Outline each Babesia divergens-infected red blood cell.
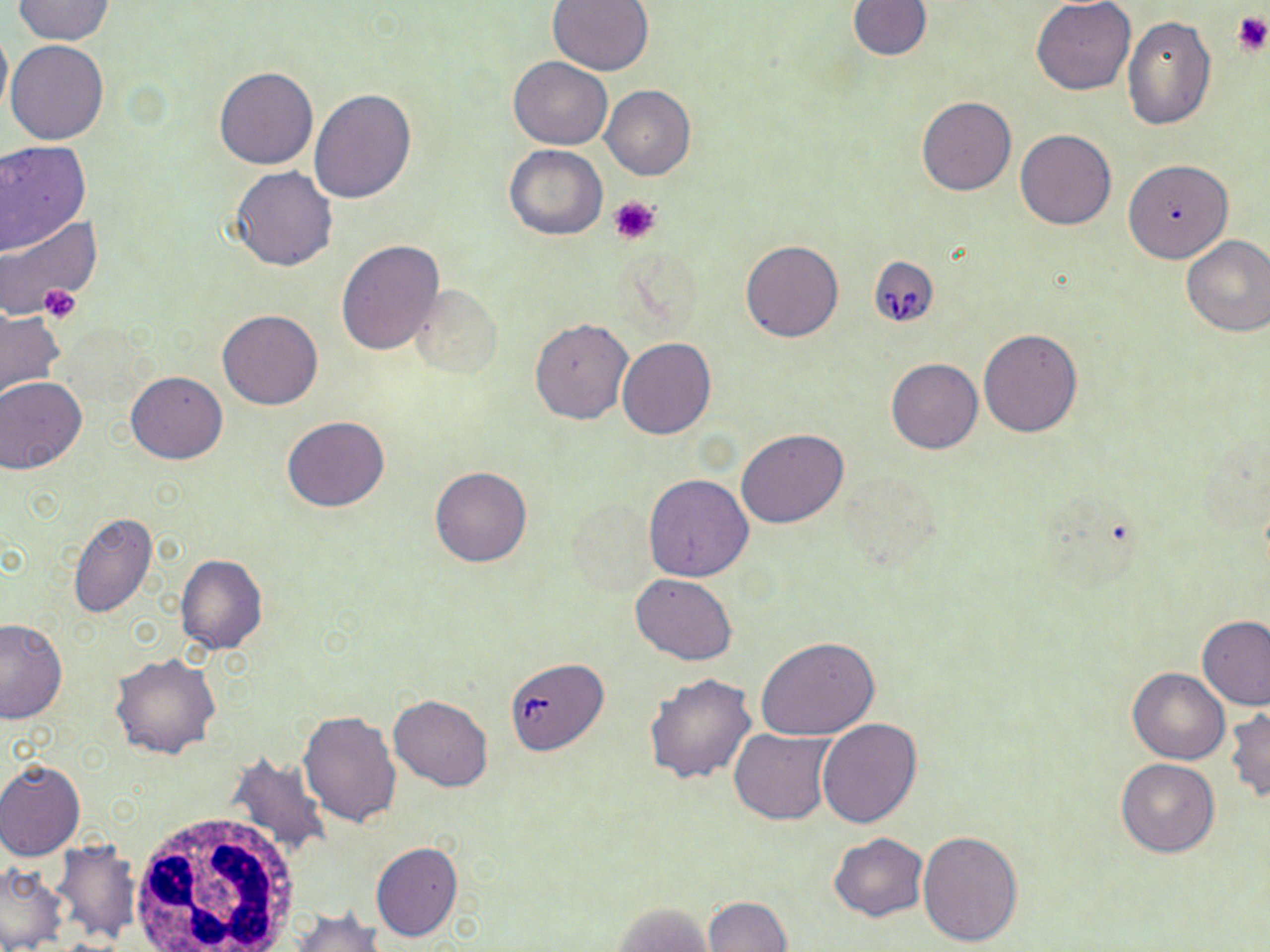
Approximate bounding boxes as named x1/y1/x2/y2 corners in pixels.
Babesia divergens-infected red blood cells: (x1=868, y1=256, x2=939, y2=328).

slide-level diagnosis = Babesia divergens
stain = May-Grünwald-Giemsa
platelet locations = approximate bounding boxes as named x1/y1/x2/y2 corners in pixels: (x1=1232, y1=10, x2=1269, y2=57), (x1=611, y1=196, x2=660, y2=244), (x1=37, y1=284, x2=82, y2=323)
field of view = single
modality = light microscopy
magnification = 1000x
uninfected red blood cell locations = approximate bounding boxes as named x1/y1/x2/y2 corners in pixels: (x1=849, y1=0, x2=932, y2=61), (x1=12, y1=1, x2=113, y2=45), (x1=546, y1=1, x2=654, y2=75), (x1=1031, y1=1, x2=1135, y2=96), (x1=1121, y1=17, x2=1216, y2=131), (x1=0, y1=23, x2=11, y2=127), (x1=6, y1=39, x2=109, y2=145), (x1=508, y1=56, x2=614, y2=149), (x1=214, y1=67, x2=317, y2=170), (x1=601, y1=85, x2=695, y2=180), (x1=309, y1=89, x2=417, y2=205), (x1=916, y1=96, x2=1016, y2=196), (x1=1015, y1=129, x2=1117, y2=230), (x1=0, y1=140, x2=90, y2=254), (x1=504, y1=144, x2=607, y2=241), (x1=1123, y1=160, x2=1232, y2=263), (x1=229, y1=166, x2=338, y2=271), (x1=0, y1=215, x2=105, y2=323), (x1=1180, y1=235, x2=1270, y2=338), (x1=740, y1=238, x2=844, y2=343), (x1=336, y1=239, x2=444, y2=355), (x1=411, y1=284, x2=500, y2=378), (x1=0, y1=306, x2=66, y2=401), (x1=217, y1=309, x2=324, y2=410), (x1=530, y1=318, x2=631, y2=424), (x1=979, y1=329, x2=1082, y2=437), (x1=616, y1=337, x2=715, y2=440), (x1=886, y1=357, x2=983, y2=454), (x1=126, y1=370, x2=228, y2=464), (x1=0, y1=377, x2=87, y2=475), (x1=282, y1=416, x2=391, y2=513), (x1=736, y1=427, x2=850, y2=528), (x1=430, y1=466, x2=531, y2=567), (x1=643, y1=474, x2=755, y2=582), (x1=68, y1=510, x2=158, y2=619), (x1=175, y1=554, x2=268, y2=655), (x1=631, y1=574, x2=737, y2=666), (x1=1197, y1=615, x2=1269, y2=710), (x1=0, y1=617, x2=68, y2=724), (x1=756, y1=638, x2=880, y2=741), (x1=111, y1=652, x2=222, y2=759), (x1=511, y1=661, x2=616, y2=758), (x1=1128, y1=668, x2=1229, y2=764), (x1=643, y1=673, x2=756, y2=785), (x1=389, y1=694, x2=493, y2=790), (x1=1226, y1=704, x2=1269, y2=801), (x1=298, y1=708, x2=401, y2=826), (x1=816, y1=717, x2=922, y2=828), (x1=727, y1=728, x2=836, y2=824), (x1=225, y1=751, x2=333, y2=860), (x1=1115, y1=757, x2=1220, y2=857), (x1=0, y1=759, x2=84, y2=861), (x1=917, y1=831, x2=1023, y2=947), (x1=829, y1=833, x2=928, y2=922), (x1=51, y1=842, x2=142, y2=943), (x1=370, y1=842, x2=463, y2=943), (x1=0, y1=862, x2=67, y2=951), (x1=702, y1=896, x2=793, y2=951), (x1=610, y1=903, x2=714, y2=951), (x1=286, y1=907, x2=386, y2=952)
white blood cell locations = approximate bounding boxes as named x1/y1/x2/y2 corners in pixels: (x1=126, y1=812, x2=300, y2=951)
preparation = thin blood film
image size = 1270×952 pixels